Give the preparation type.
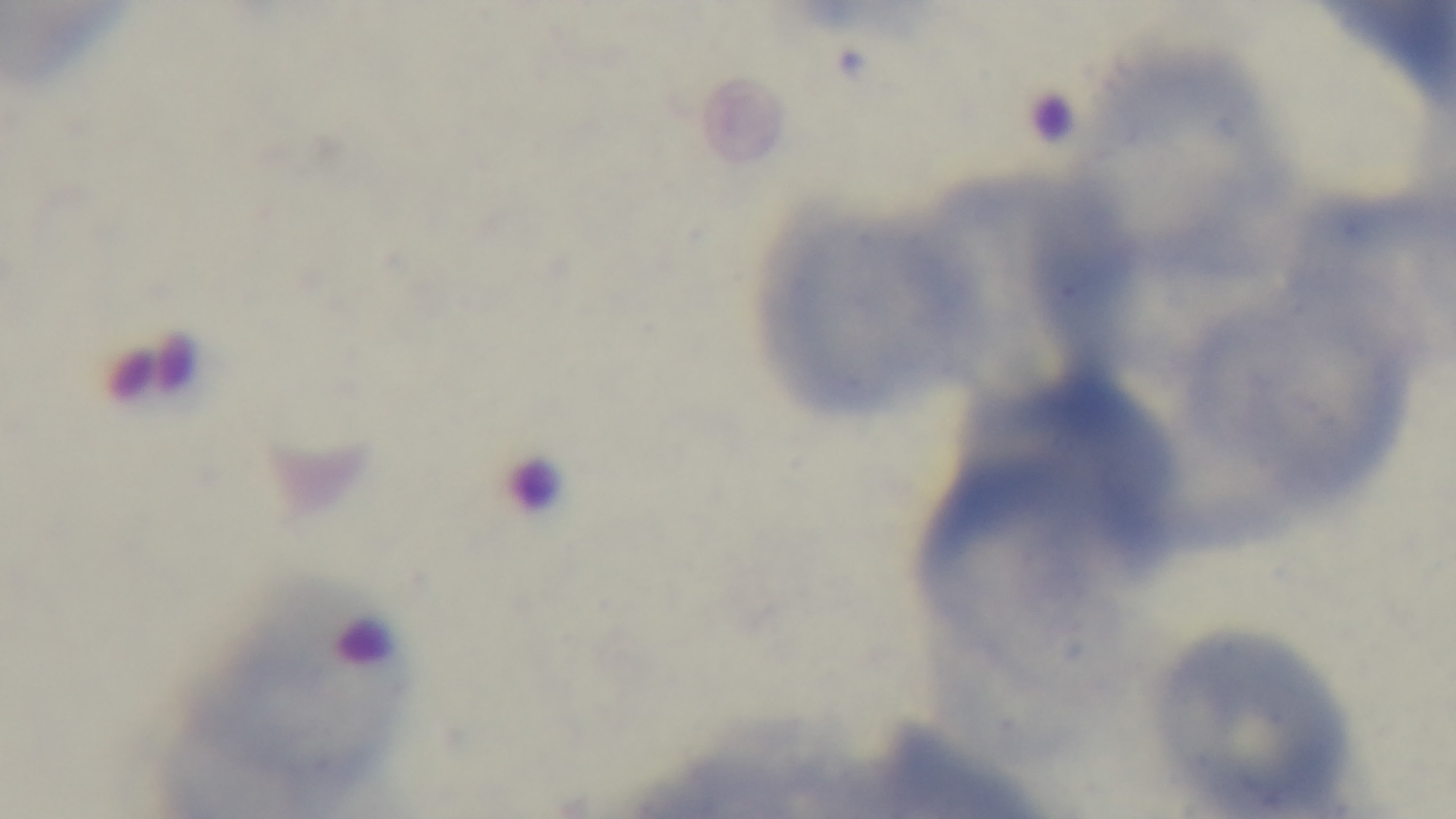

Thin.

malaria status = negative
objective = 100x oil immersion
capture = mounted 4K digital camera
stain = Giemsa
field of view = single
modality = light microscopy